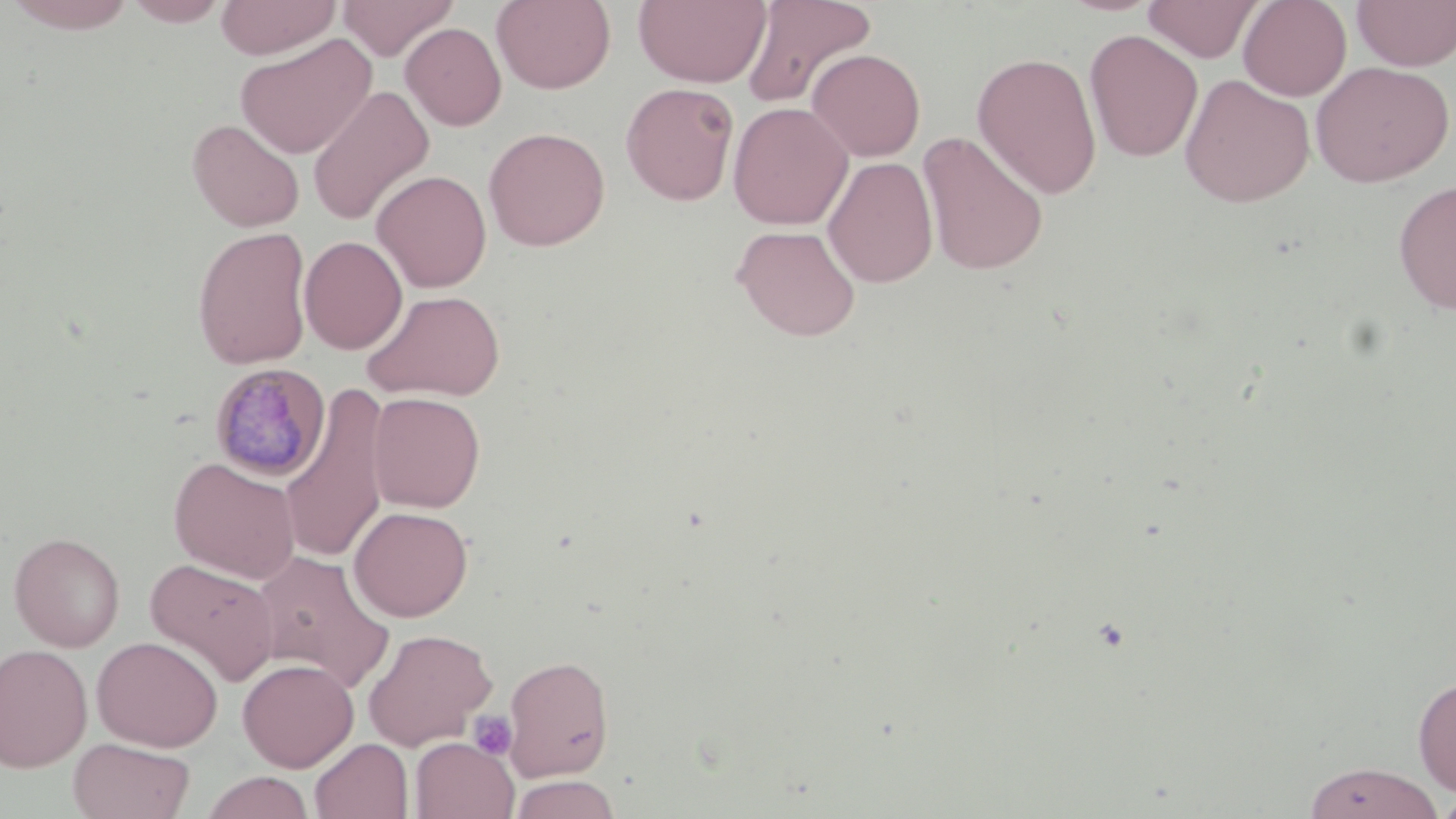

Approximate bounding boxes as (x1, y1, x2, y2) in pixels. Uninfected red blood cell locations: (1, 0, 141, 33), (122, 0, 233, 26), (215, 0, 341, 60), (336, 0, 458, 61), (491, 0, 616, 93), (633, 0, 771, 88), (740, 0, 878, 109), (1238, 0, 1352, 101), (1352, 0, 1456, 70), (1143, 1, 1264, 62), (400, 22, 507, 131), (1083, 30, 1203, 162), (235, 33, 376, 159), (807, 49, 926, 162), (972, 51, 1103, 199), (1310, 61, 1454, 187), (1179, 73, 1315, 207), (620, 82, 739, 206), (307, 85, 434, 226), (728, 102, 853, 230), (187, 118, 304, 232), (483, 126, 611, 251), (917, 131, 1050, 276), (823, 156, 938, 289), (371, 170, 492, 292), (1393, 179, 1456, 315), (731, 224, 861, 342), (192, 226, 313, 370), (299, 236, 407, 354), (361, 289, 505, 402), (282, 386, 391, 564), (367, 391, 486, 512), (168, 456, 301, 583), (349, 505, 474, 622), (8, 532, 125, 652), (250, 550, 393, 692), (145, 557, 280, 687), (362, 627, 497, 749), (92, 635, 223, 752), (0, 644, 93, 771), (502, 654, 615, 781), (237, 658, 358, 772), (1413, 675, 1456, 796), (68, 737, 195, 819), (410, 737, 519, 819), (310, 739, 414, 819), (1303, 762, 1445, 819), (200, 771, 315, 819), (509, 774, 621, 819), (1435, 791, 1456, 818). Platelet locations: (468, 710, 518, 760). Plasmodium malariae-infected red blood cell locations: (209, 363, 331, 482). Slide-level diagnosis: Plasmodium malariae. 1000x magnification. Thin blood smear. May-Grünwald-Giemsa stain. Image is 1456×819 pixels. One field of a larger specimen. Optical microscopy.